Report the malaria status of this cell.
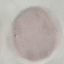
It is uninfected.

Cell patch, automatically extracted from a larger field of view and resized to 64 × 64 pixels. Thin blood film. Acquired by smartphone through the microscope eyepiece. Giemsa stain.